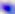

Summary:
  - Identification: Toxoplasma gondii
  - Modality: photomicrograph
  - Magnification: 400x